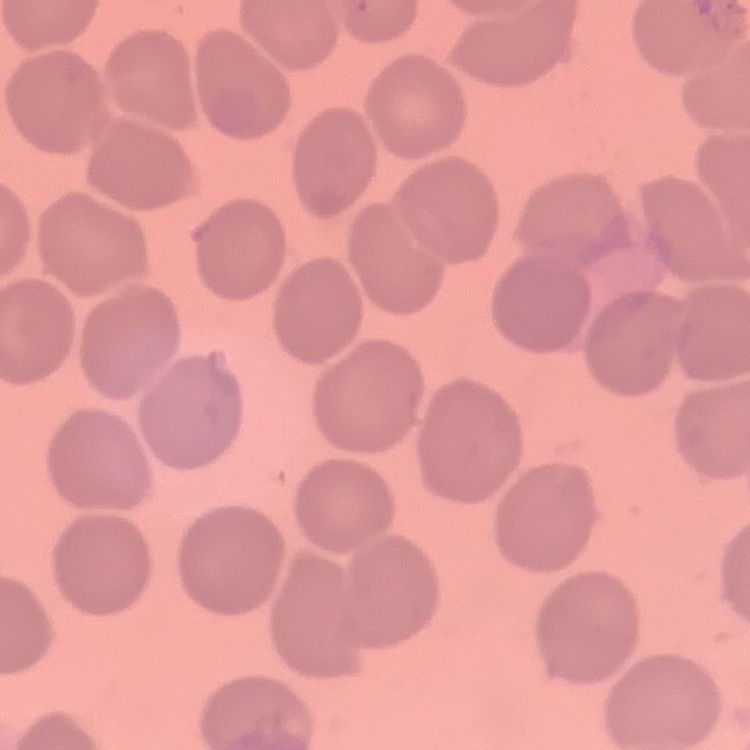 The erythrocytes show no rouleaux formation. Thin peripheral smear. Field's or Giemsa stain. Square crop of a larger photomicrograph.